Classify this cell by malaria status.
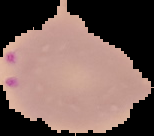
It is parasitized.

Summary:
  - Image size: 154×136 pixels
  - Image type: segmented cell region with the area outside set to black
  - Preparation: thin blood film